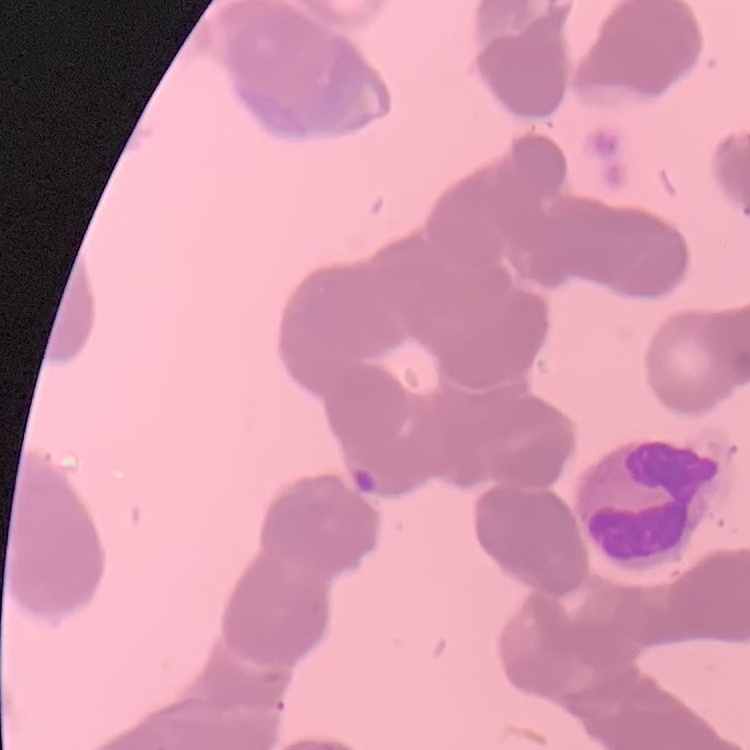

The erythrocytes show rouleaux formation. Stained with either Field's or Giemsa. Thin blood film. Square crop of a larger photomicrograph.